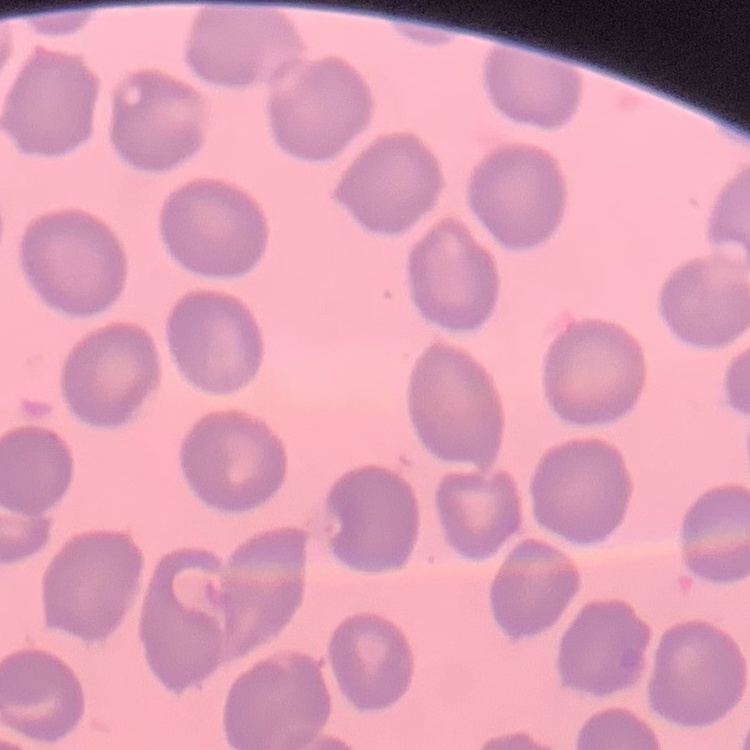

The erythrocytes show no rouleaux formation. Thin peripheral smear. Field's or Giemsa stain. One tile cut from a larger photomicrograph.